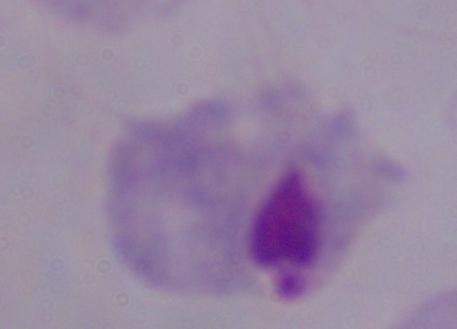 Captured at 1000x magnification. Micrograph. A trichomonad is shown.